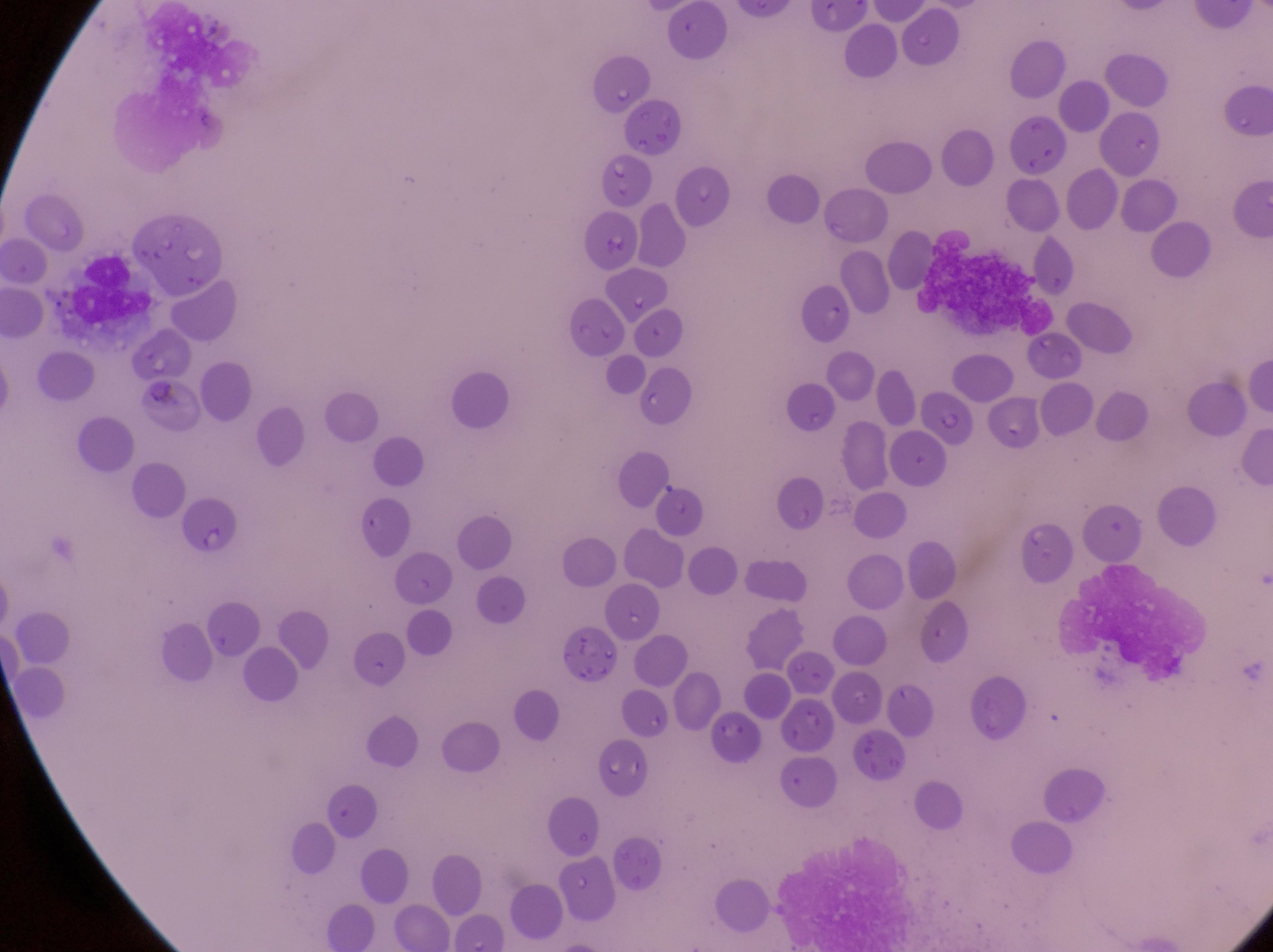
image size = 1273×952 pixels
preparation = thin blood smear
field of view = single
parasitised red blood cell locations = approximate bounding boxes as {left, top, right, bottom} in pixels: {582, 210, 639, 273}, {799, 285, 851, 347}, {567, 295, 630, 358}, {911, 387, 976, 445}, {175, 495, 242, 563}
capture = smartphone photograph through the eyepiece of an Olympus CX-23 microscope
magnification = 1000x
country = Uganda
leukocyte locations = approximate bounding boxes as {left, top, right, bottom} in pixels: {922, 229, 1053, 326}, {67, 247, 164, 334}